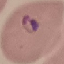
malaria status = parasitized
preparation = thin blood film
stain = Giemsa
image type = cell patch, automatically extracted from a larger field of view and resized to 64 × 64 pixels
capture = smartphone camera at the microscope eyepiece